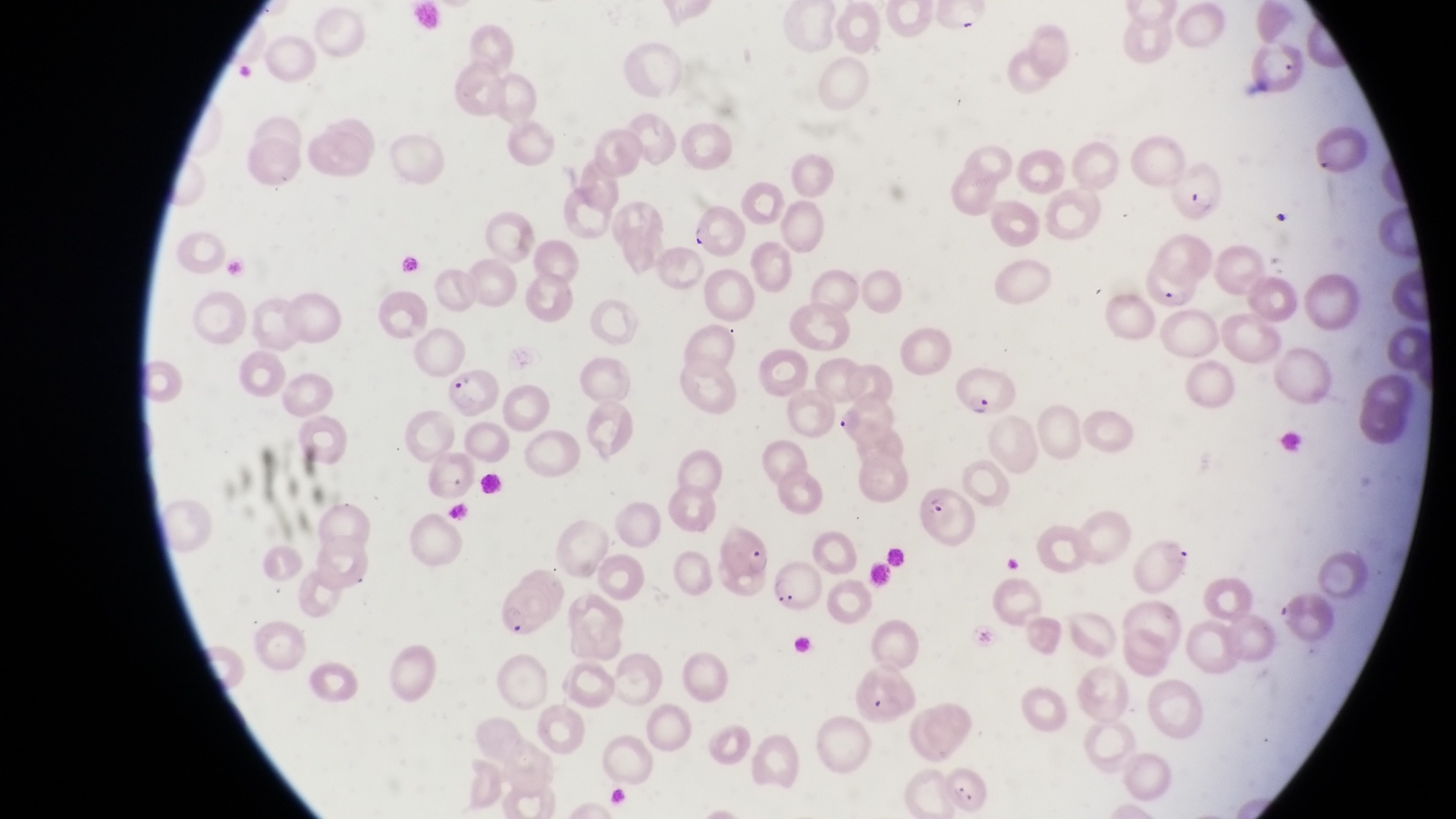

{
  "capture": "smartphone photograph through the eyepiece of an Olympus CX-23 microscope",
  "preparation": "thin blood smear",
  "field_of_view": "single",
  "magnification": "1000x",
  "country": "Uganda",
  "parasitised_red_blood_cell_locations": "approximate bounding boxes as (left, top, right, bottom) in pixels: (1168, 159, 1228, 222), (1136, 251, 1197, 310), (441, 366, 501, 419), (952, 366, 1015, 416), (915, 482, 976, 548), (717, 525, 775, 580), (1133, 534, 1194, 594), (769, 562, 827, 614)",
  "image_size": "1456×819 pixels"
}